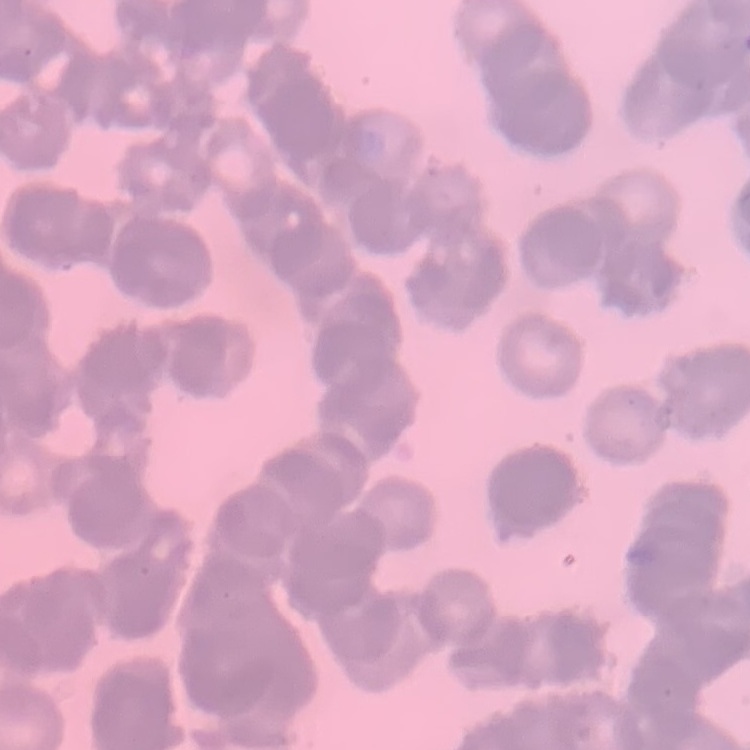
Summary:
  - Erythrocyte morphology: rouleaux formation
  - Image type: square crop of a larger photomicrograph
  - Preparation: thin peripheral smear
  - Stain: Field's or Giemsa